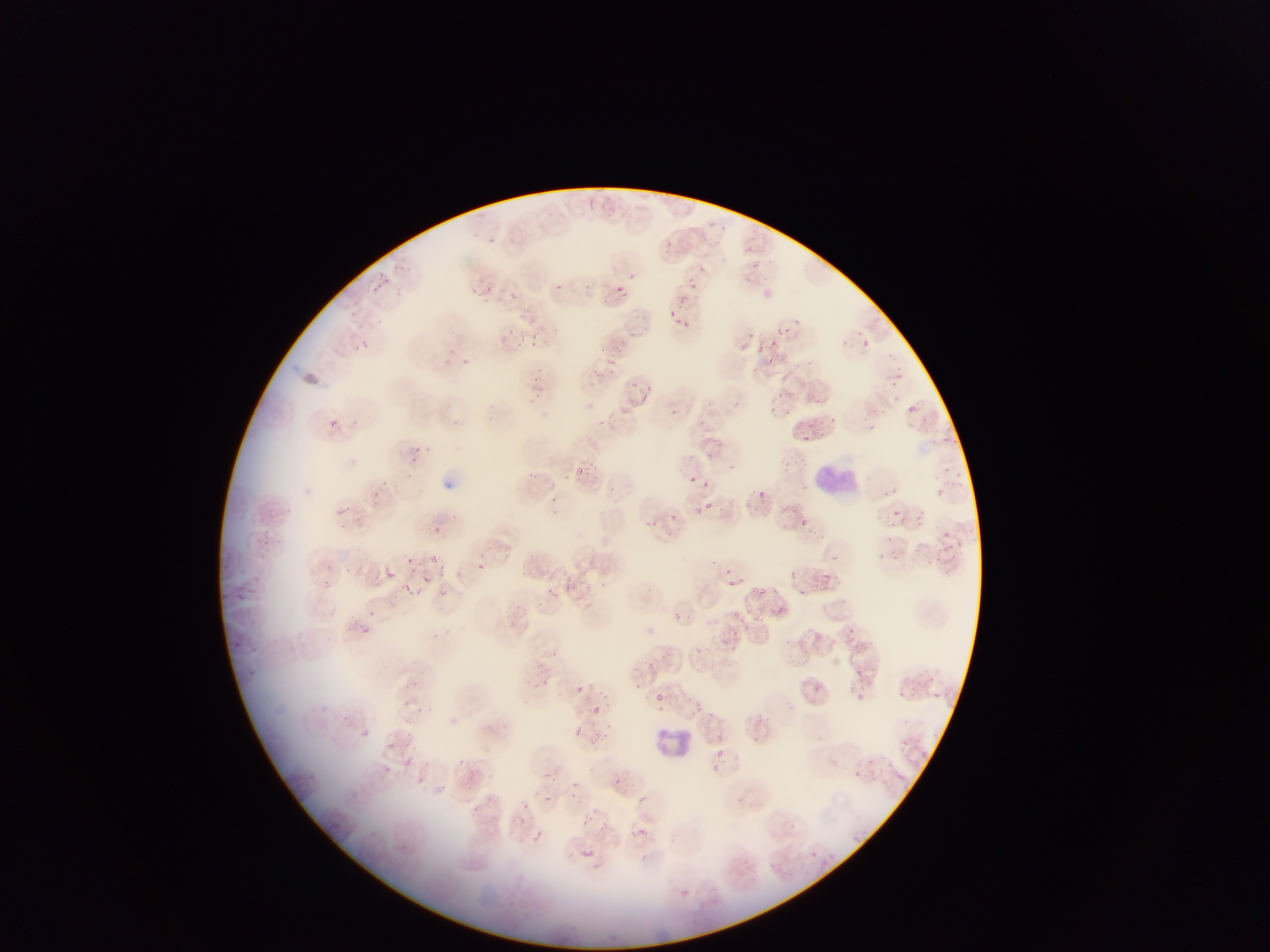

Approximate bounding boxes as (left, top, right, bottom) in pixels. Malaria parasite locations: (706, 210, 730, 231), (701, 230, 713, 244), (746, 237, 761, 261), (623, 270, 650, 287), (372, 275, 390, 290), (688, 277, 701, 290), (555, 281, 562, 292), (613, 282, 630, 298), (486, 285, 497, 293), (762, 289, 777, 297), (673, 305, 716, 334), (795, 314, 803, 323), (507, 319, 525, 334), (529, 322, 551, 346), (624, 323, 643, 347), (753, 330, 786, 356), (359, 340, 372, 351), (861, 340, 871, 348), (600, 351, 618, 364), (461, 357, 475, 377), (892, 365, 905, 383), (535, 373, 551, 388), (636, 377, 660, 405), (773, 390, 784, 396), (816, 395, 827, 405), (610, 396, 647, 422), (771, 404, 781, 416), (907, 404, 919, 413), (328, 417, 339, 428), (797, 420, 829, 449), (931, 424, 952, 447), (412, 445, 421, 453), (777, 453, 810, 480), (575, 460, 591, 476), (954, 462, 974, 499), (526, 466, 548, 490), (691, 475, 705, 486), (930, 478, 951, 500), (372, 485, 390, 510), (759, 492, 767, 496), (552, 496, 567, 507), (748, 496, 765, 514), (691, 499, 709, 517), (708, 505, 720, 515), (906, 505, 929, 529), (788, 508, 812, 527), (892, 508, 901, 517), (805, 513, 821, 523), (636, 516, 673, 545), (943, 528, 969, 562), (884, 535, 908, 557), (430, 551, 440, 562), (404, 552, 420, 572), (476, 557, 488, 570), (385, 564, 399, 580), (439, 564, 448, 578), (720, 565, 730, 578), (576, 566, 588, 574), (787, 570, 802, 581), (418, 573, 431, 583), (567, 575, 583, 589), (722, 575, 742, 589), (816, 576, 840, 604), (322, 578, 341, 596), (400, 582, 414, 595), (602, 582, 609, 590), (548, 584, 564, 606), (754, 586, 773, 599), (440, 587, 450, 598), (743, 597, 752, 609), (775, 607, 785, 616), (367, 609, 375, 617), (733, 609, 752, 623), (844, 627, 863, 642), (798, 640, 816, 660), (728, 641, 750, 652), (694, 644, 705, 659), (644, 659, 668, 678), (857, 668, 865, 678), (921, 673, 940, 690), (570, 682, 589, 702), (811, 682, 826, 702), (841, 682, 871, 705), (885, 683, 908, 698), (408, 686, 431, 701), (655, 693, 665, 701), (590, 697, 609, 718), (693, 697, 711, 719), (405, 711, 426, 723), (571, 723, 600, 746), (362, 729, 371, 737), (660, 729, 667, 737), (899, 733, 921, 749), (402, 734, 422, 749), (376, 738, 401, 760), (715, 744, 730, 764), (857, 753, 887, 773), (392, 755, 409, 772), (403, 757, 426, 770), (896, 773, 904, 780), (543, 792, 552, 801), (637, 796, 646, 804), (522, 802, 530, 810), (580, 816, 591, 826), (638, 822, 657, 840), (533, 827, 560, 860), (580, 847, 602, 866). Leukocyte locations: (816, 456, 855, 503), (652, 731, 697, 762). Photographed through a microscope with a mobile-phone camera. Sample from Ghana. Image is 1270×952 pixels. One field of view. Thin blood smear.